Assess the morphology of the red blood cells.
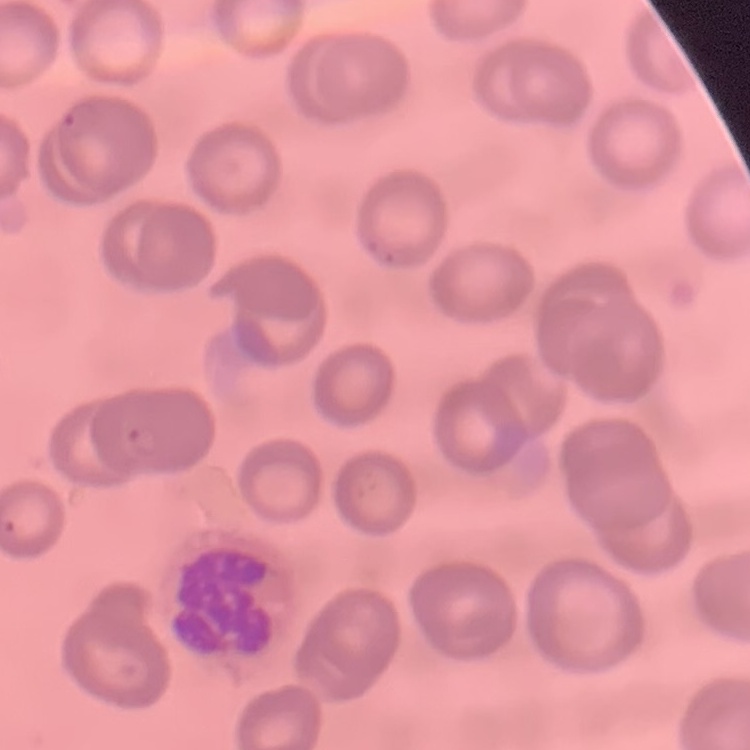
They show no rouleaux formation.

image type = square crop of a larger photomicrograph
stain = Field's or Giemsa
preparation = thin blood film